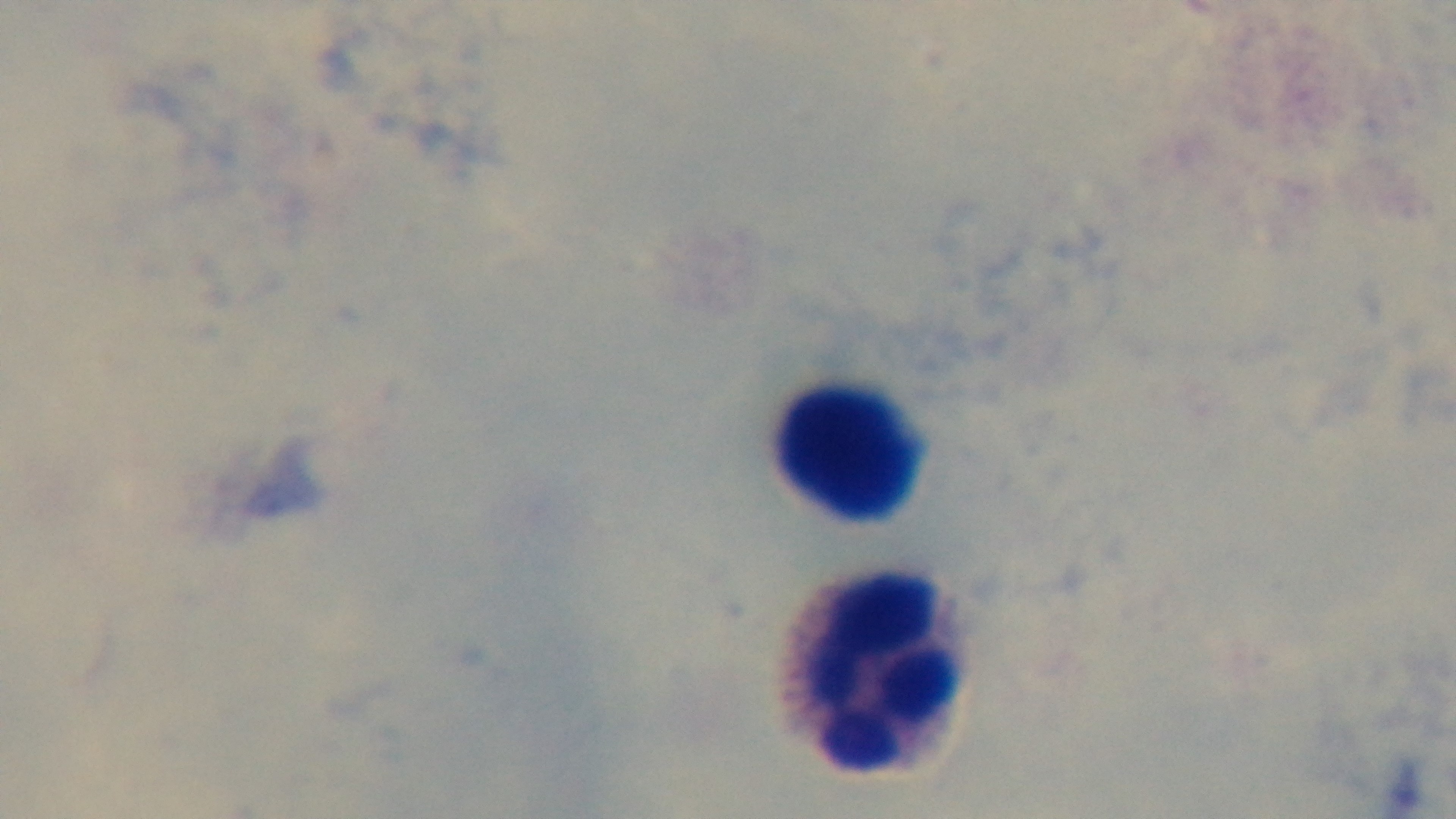

Giemsa stain. Mounted 4K digital camera. Single field of view. Preparation: thick blood film. Malaria status: uninfected. 100x oil-immersion objective. Photomicrograph.